Assess this cell for malaria.
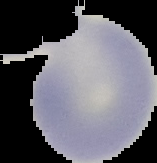
It is uninfected.

Summary:
  - Image type: segmented cell region with the area outside set to black
  - Preparation: thin blood smear
  - Image size: 157×163 pixels